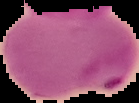

Image is 139×103 pixels. From a thin blood film. Cell region segmented out of the field of view; the surrounding area is masked to black. Malaria status: parasitized.